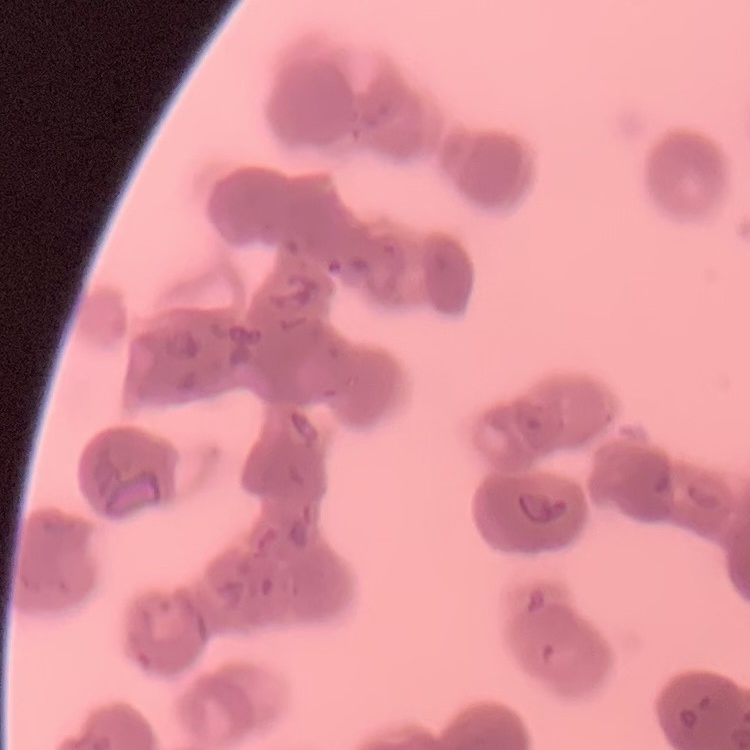
red blood cell morphology = rouleaux formation
stain = Field's or Giemsa
image type = square crop of a larger photomicrograph
preparation = thin blood film